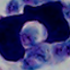

{
  "identification": "leukocyte",
  "magnification": "1000x",
  "modality": "photomicrograph"
}